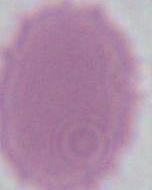

modality: photomicrograph
magnification: 1000x
identification: erythrocyte